State the blood parasite species.
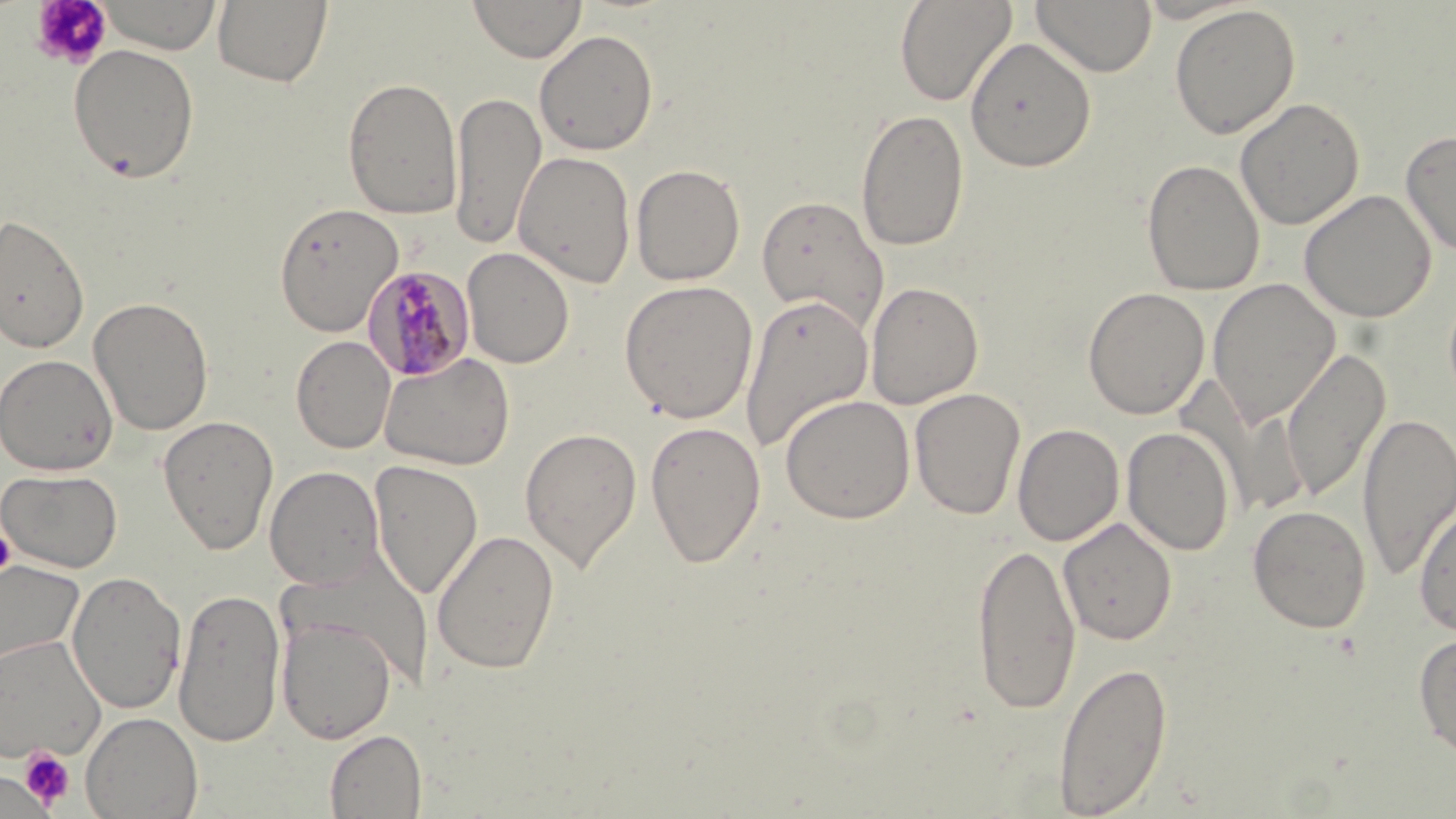
Plasmodium malariae.

Approximate bounding boxes as (x1, y1, x2, y2) in pixels. Platelet locations: (28, 0, 114, 71), (1, 524, 16, 579), (19, 748, 75, 808), (1, 770, 52, 818). Plasmodium malariae-infected red blood cell locations: (363, 264, 475, 382). Uninfected red blood cell locations: (97, 0, 224, 55), (212, 0, 333, 88), (468, 0, 587, 63), (894, 0, 1016, 107), (1031, 0, 1157, 77), (1169, 4, 1300, 139), (534, 29, 659, 156), (965, 36, 1097, 172), (67, 44, 201, 183), (342, 77, 463, 220), (450, 90, 546, 250), (1235, 98, 1365, 230), (856, 108, 970, 252), (1400, 128, 1456, 258), (514, 151, 636, 288), (1141, 158, 1265, 296), (630, 164, 746, 286), (1299, 190, 1437, 323), (755, 194, 890, 334), (274, 202, 403, 337), (0, 212, 90, 354), (462, 247, 574, 368), (1207, 278, 1340, 427), (619, 280, 758, 422), (865, 281, 984, 408), (1083, 287, 1210, 419), (740, 293, 873, 453), (89, 295, 214, 435), (291, 335, 396, 453), (1280, 348, 1391, 503), (379, 352, 515, 471), (0, 353, 118, 475), (909, 388, 1026, 520), (780, 394, 915, 524), (1357, 411, 1456, 580), (158, 415, 279, 555), (644, 420, 766, 568), (1012, 423, 1125, 546), (519, 427, 642, 573), (1122, 427, 1235, 556), (368, 459, 484, 599), (265, 465, 384, 590), (1, 468, 124, 573), (1413, 499, 1456, 637), (1247, 504, 1371, 633), (1058, 517, 1177, 645), (431, 528, 560, 675), (971, 541, 1081, 714), (0, 559, 85, 669), (66, 570, 187, 715), (172, 587, 286, 748), (276, 616, 396, 744), (1413, 632, 1456, 759), (0, 635, 106, 762), (1053, 660, 1173, 816), (81, 711, 203, 819), (324, 730, 426, 818), (0, 769, 54, 817). Thin blood smear. 1000x magnification. Image is 1456×819 pixels. Optical microscopy. May-Grünwald-Giemsa stain. One field of a larger specimen.